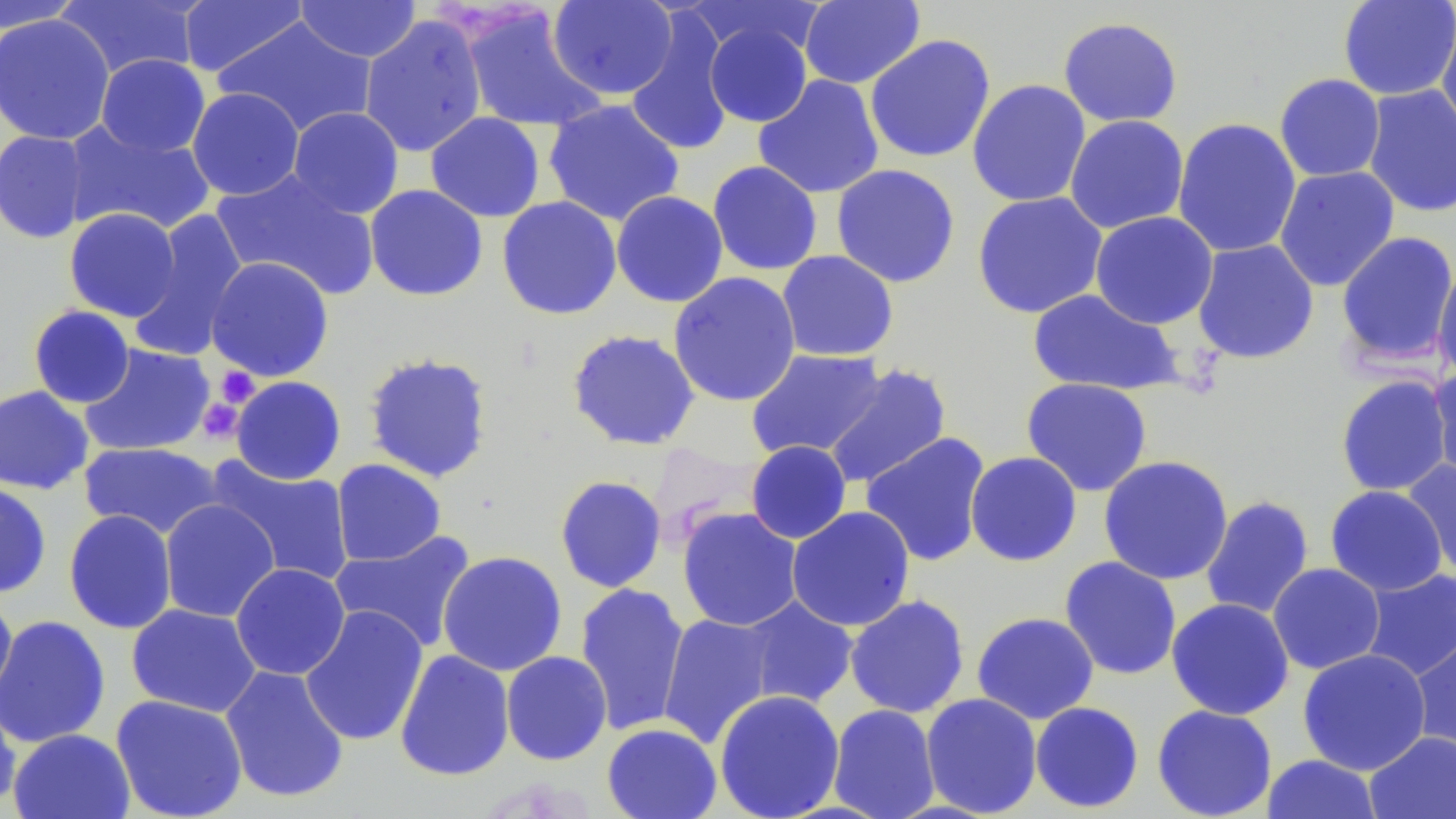

Summary:
  - Coordinate format: approximate bounding boxes as [x1, y1, x2, y2] in pixels
  - Platelet locations: [215, 366, 260, 408], [196, 398, 245, 444]
  - Uninfected red blood cell locations: [0, 0, 88, 34], [56, 0, 203, 80], [547, 0, 678, 100], [686, 0, 824, 59], [1338, 0, 1456, 101], [177, 1, 308, 77], [295, 1, 422, 62], [799, 1, 925, 89], [460, 7, 607, 134], [624, 11, 735, 156], [0, 13, 115, 146], [359, 14, 488, 158], [1436, 15, 1456, 142], [213, 16, 378, 137], [1057, 16, 1184, 128], [703, 20, 813, 128], [865, 34, 996, 163], [96, 54, 210, 157], [1274, 73, 1386, 182], [753, 75, 884, 199], [967, 79, 1092, 207], [1362, 84, 1456, 218], [187, 87, 304, 200], [543, 99, 685, 227], [287, 106, 404, 218], [425, 112, 545, 222], [1064, 115, 1189, 234], [1172, 117, 1302, 259], [63, 120, 215, 236], [0, 130, 90, 244], [707, 160, 823, 276], [831, 163, 961, 288], [1274, 165, 1400, 291], [212, 169, 380, 300], [364, 184, 488, 302], [611, 191, 728, 308], [972, 191, 1109, 319], [496, 196, 622, 320], [64, 207, 181, 322], [130, 208, 249, 361], [1090, 211, 1218, 329], [1335, 231, 1456, 368], [1191, 238, 1320, 364], [776, 250, 899, 362], [206, 256, 334, 382], [1432, 259, 1456, 384], [668, 271, 802, 407], [1027, 288, 1183, 396], [28, 305, 135, 408], [566, 329, 701, 451], [79, 344, 216, 457], [745, 348, 888, 461], [362, 351, 494, 483], [823, 364, 952, 489], [1428, 364, 1456, 484], [1334, 374, 1454, 497], [230, 376, 346, 485], [1021, 377, 1153, 496], [0, 385, 94, 495], [860, 432, 991, 566], [745, 440, 852, 544], [78, 442, 223, 540], [965, 451, 1083, 566], [1098, 455, 1234, 585], [206, 456, 355, 587], [330, 459, 447, 566], [1401, 460, 1455, 582], [554, 475, 667, 593], [0, 481, 52, 598], [1324, 485, 1448, 596], [1200, 495, 1314, 620], [159, 499, 281, 623], [786, 506, 916, 632], [677, 507, 803, 632], [63, 509, 178, 634], [329, 529, 477, 653], [437, 550, 567, 676], [1059, 556, 1182, 680], [230, 563, 350, 680], [1267, 563, 1385, 674], [1359, 568, 1456, 681], [574, 582, 690, 736], [0, 591, 17, 704], [844, 594, 970, 718], [738, 597, 859, 709], [1166, 597, 1295, 720], [126, 603, 261, 718], [299, 605, 429, 747], [971, 611, 1099, 724], [657, 612, 779, 748], [0, 615, 111, 748], [1409, 628, 1456, 760], [1297, 648, 1431, 776], [394, 649, 515, 781], [501, 651, 612, 765], [220, 665, 350, 804], [714, 689, 845, 818], [921, 693, 1043, 817], [110, 694, 248, 819], [0, 699, 21, 814], [1030, 701, 1144, 813], [827, 704, 941, 819], [1151, 704, 1278, 819], [601, 723, 722, 819], [8, 728, 136, 818], [1364, 731, 1456, 819], [1261, 754, 1384, 818]
  - Slide-level diagnosis: no evidence of blood parasites
  - Image size: 1456×819 pixels
  - Modality: light microscopy
  - Preparation: thin blood film
  - Field of view: one of a larger specimen
  - Stain: May-Grünwald-Giemsa
  - Magnification: 1000x